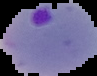
preparation = thin blood film
image type = cell region segmented out of the field of view; surrounding area masked to black
image size = 97×76 pixels
result = Plasmodium parasites detected